Outline each blood parasite and name the species.
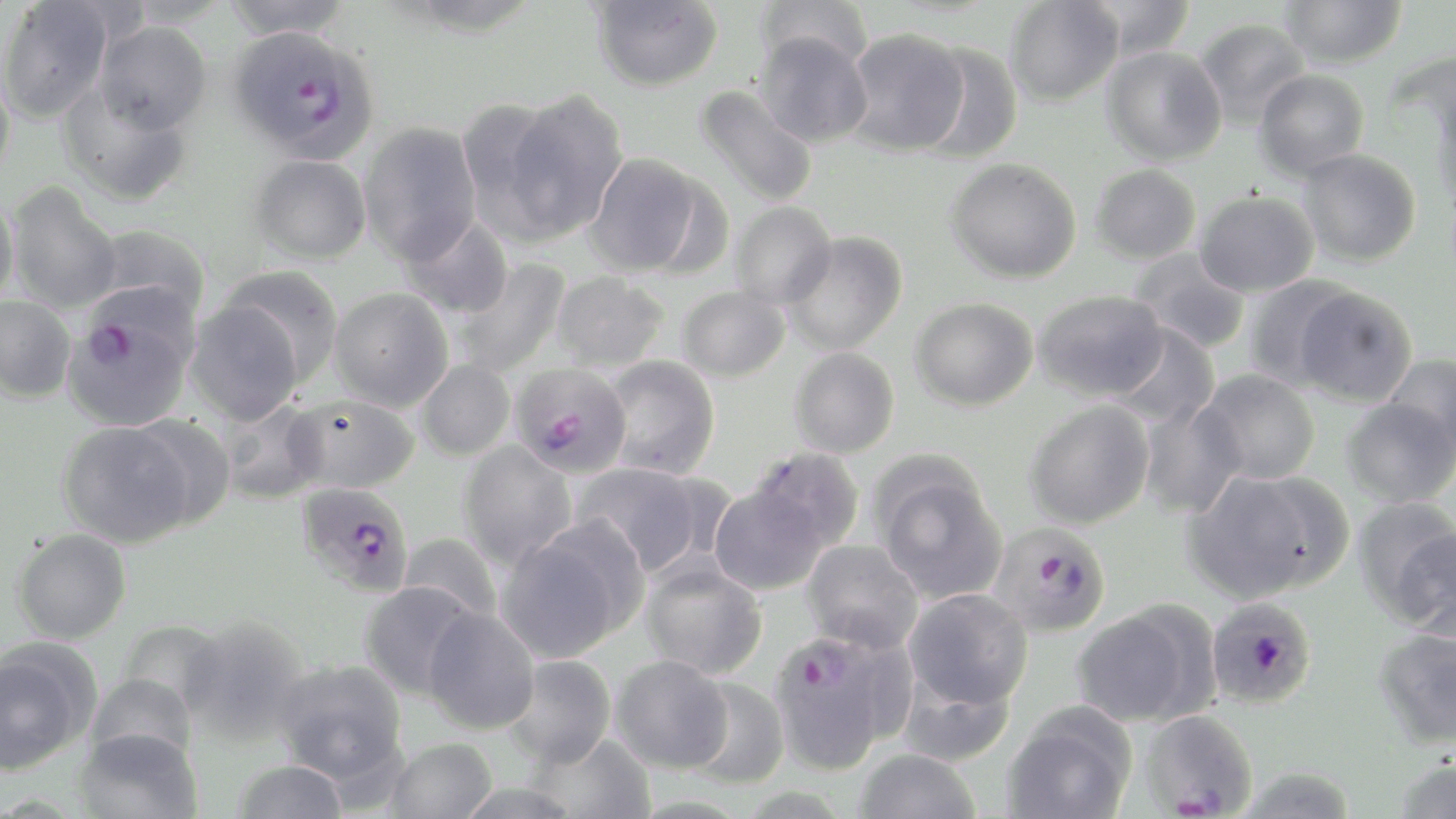
Approximate bounding boxes as (x1, y1, x2, y2) in pixels.
Plasmodium falciparum-infected red blood cells: (226, 24, 380, 164), (62, 300, 195, 432), (510, 362, 633, 478), (295, 482, 414, 597), (989, 522, 1113, 637), (1206, 597, 1317, 708), (767, 630, 907, 774), (1139, 708, 1260, 817).
No Plasmodium ovale, Plasmodium malariae, Plasmodium vivax, Babesia divergens, or Trypanosoma brucei observed.

Uninfected red blood cell locations: (221, 0, 353, 40), (753, 0, 873, 75), (1081, 0, 1196, 60), (1280, 0, 1408, 70), (0, 1, 116, 124), (590, 1, 723, 92), (1004, 1, 1123, 107), (1194, 18, 1310, 130), (92, 21, 212, 135), (843, 28, 970, 155), (753, 32, 873, 147), (915, 43, 1023, 163), (1101, 46, 1227, 166), (0, 68, 16, 186), (1254, 69, 1369, 181), (59, 84, 193, 207), (694, 85, 819, 208), (494, 90, 628, 243), (359, 122, 482, 265), (1297, 148, 1422, 266), (584, 152, 710, 278), (249, 154, 371, 265), (945, 158, 1083, 284), (1090, 164, 1202, 265), (6, 183, 122, 313), (1194, 190, 1319, 297), (0, 193, 19, 306), (730, 201, 837, 308), (399, 214, 514, 320), (92, 223, 211, 321), (782, 232, 908, 356), (1127, 248, 1251, 355), (453, 258, 571, 378), (220, 265, 344, 387), (552, 271, 670, 372), (1242, 275, 1357, 389), (677, 286, 790, 382), (1293, 286, 1418, 406), (328, 288, 454, 412), (1032, 289, 1169, 402), (0, 296, 76, 404), (909, 297, 1039, 412), (184, 300, 305, 426), (1108, 324, 1220, 428), (789, 347, 900, 458), (1381, 354, 1456, 455), (601, 355, 721, 480), (416, 359, 516, 461), (1196, 369, 1320, 485), (289, 395, 421, 494), (1341, 397, 1455, 509), (1024, 399, 1155, 530), (1137, 399, 1246, 519), (218, 400, 327, 505), (126, 414, 237, 530), (57, 421, 196, 549), (458, 441, 577, 570), (748, 446, 866, 556), (869, 455, 1007, 605), (571, 462, 712, 578), (1185, 467, 1349, 602), (708, 480, 831, 597), (1352, 496, 1455, 624), (495, 521, 643, 663), (1389, 527, 1456, 640), (11, 528, 131, 644), (398, 531, 502, 626), (802, 540, 924, 652), (639, 558, 767, 680), (359, 581, 481, 700), (902, 588, 1033, 712), (1071, 605, 1209, 727), (422, 606, 540, 734), (179, 616, 312, 747), (118, 620, 227, 719), (1373, 626, 1456, 750), (0, 643, 93, 774), (501, 654, 617, 768), (609, 655, 733, 773), (274, 659, 409, 785), (85, 673, 198, 765), (683, 677, 790, 788), (1001, 704, 1137, 819), (74, 727, 204, 819), (526, 731, 656, 819), (385, 737, 497, 819), (855, 748, 982, 819), (1389, 756, 1456, 819), (232, 759, 349, 819). Slide-level diagnosis: Plasmodium falciparum. May-Grünwald-Giemsa stain. Captured at 1000x magnification. Image is 1456×819 pixels. Thin blood film. Light microscopy. One field of a larger specimen.